Assess this cell for malaria.
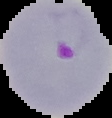
It is parasitized.

{
  "image_size": "112×118 pixels",
  "image_type": "segmented cell region on a black background",
  "preparation": "thin blood film"
}